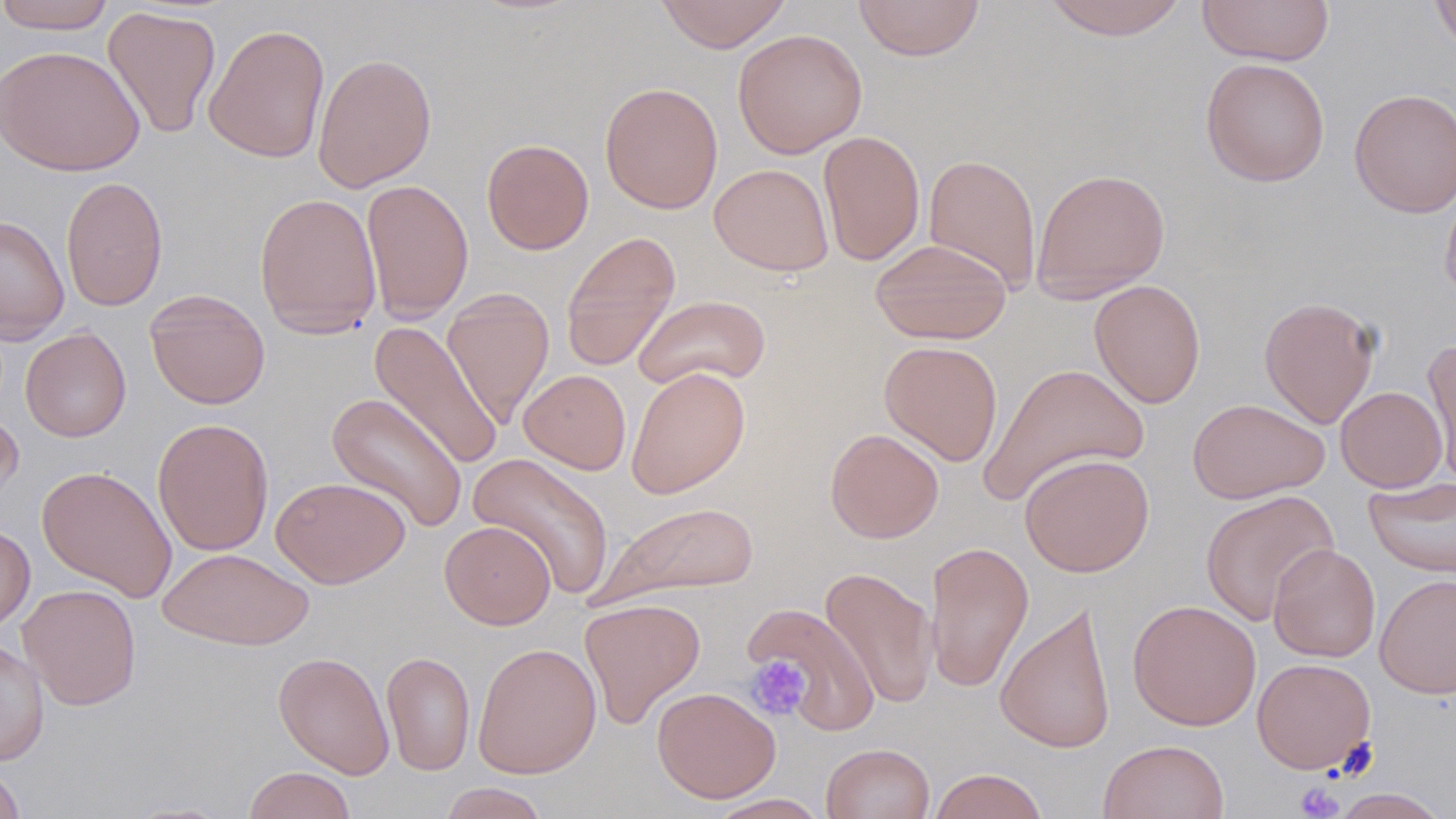

Summary:
  - Coordinate format: approximate bounding boxes as [x1, y1, x2, y2] in pixels
  - Uninfected red blood cell locations: [655, 0, 793, 52], [852, 0, 986, 61], [1042, 0, 1190, 40], [1196, 0, 1335, 66], [1430, 0, 1456, 56], [0, 1, 118, 34], [102, 6, 222, 140], [204, 23, 331, 164], [732, 28, 867, 159], [0, 45, 144, 176], [312, 52, 437, 192], [1200, 57, 1330, 186], [599, 82, 723, 214], [1349, 87, 1456, 218], [818, 130, 926, 266], [481, 138, 594, 255], [923, 153, 1042, 293], [709, 164, 834, 276], [1031, 167, 1170, 303], [60, 175, 168, 312], [360, 178, 474, 324], [1440, 181, 1456, 304], [253, 192, 382, 340], [0, 213, 69, 344], [560, 230, 681, 372], [870, 238, 1012, 344], [1089, 279, 1206, 408], [441, 287, 555, 429], [144, 289, 270, 410], [633, 294, 771, 390], [1259, 296, 1381, 428], [368, 321, 504, 470], [20, 327, 131, 442], [880, 340, 1003, 466], [1421, 342, 1456, 484], [979, 362, 1149, 507], [626, 366, 750, 499], [519, 369, 631, 474], [1336, 386, 1448, 491], [326, 393, 469, 533], [1187, 398, 1329, 504], [0, 409, 24, 520], [152, 417, 274, 556], [825, 428, 944, 543], [468, 451, 615, 600], [1019, 452, 1155, 577], [36, 466, 177, 602], [1364, 475, 1456, 578], [271, 476, 411, 588], [1200, 489, 1339, 626], [595, 500, 760, 605], [440, 520, 555, 629], [0, 522, 35, 633], [925, 540, 1034, 693], [1268, 543, 1380, 662], [158, 547, 314, 650], [820, 566, 938, 709], [1374, 574, 1456, 699], [18, 583, 142, 710], [578, 597, 706, 729], [1127, 599, 1261, 730], [995, 602, 1117, 754], [742, 603, 880, 735], [0, 639, 49, 767], [473, 642, 602, 779], [273, 651, 394, 779], [381, 651, 476, 776], [1252, 657, 1376, 773], [652, 686, 780, 803], [1097, 739, 1230, 819], [821, 743, 935, 819], [0, 765, 26, 819], [243, 766, 356, 819], [928, 768, 1049, 819], [438, 782, 550, 819], [1330, 787, 1450, 818], [706, 793, 830, 819], [117, 800, 237, 818]
  - Platelet locations: [746, 655, 812, 721], [1295, 783, 1343, 818]
  - Slide-level diagnosis: no evidence of blood parasites
  - Image size: 1456×819 pixels
  - Field of view: one of a larger specimen
  - Preparation: thin blood smear
  - Stain: May-Grünwald-Giemsa
  - Modality: optical microscopy
  - Magnification: 1000x